Comment on the morphology of the red blood cells.
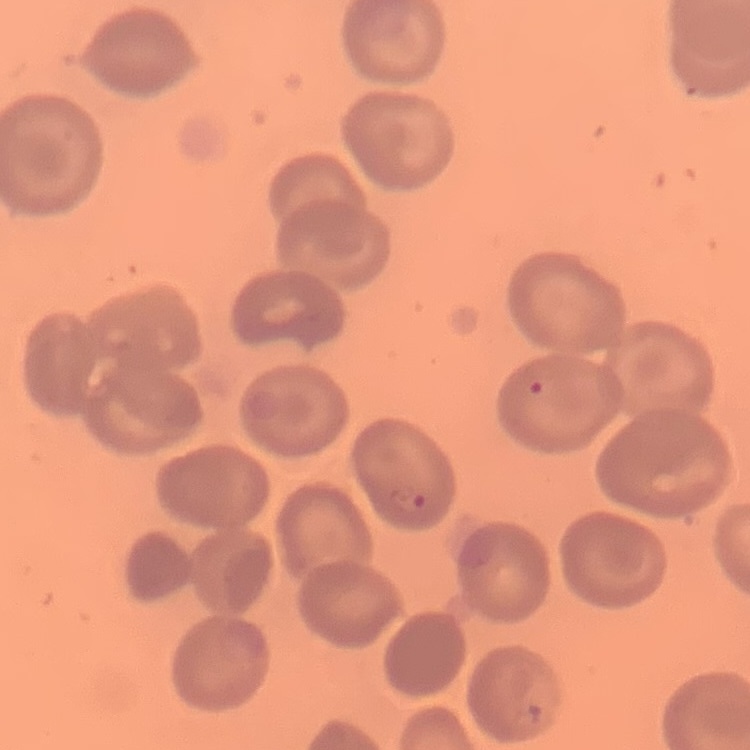
They show no rouleaux formation.

Square crop of a larger photomicrograph. Stained with either Field's or Giemsa. Thin peripheral smear.